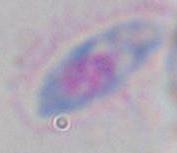

1000x magnification. Toxoplasma gondii is seen. Photomicrograph.